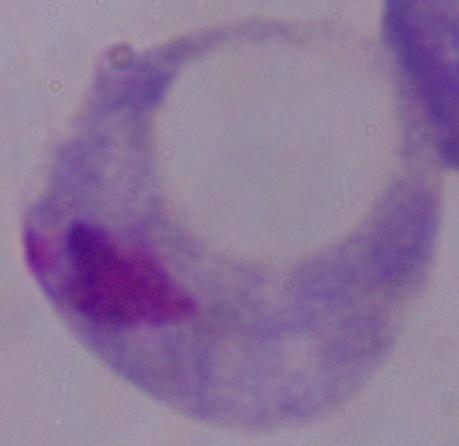
Summary:
  - Identification: trichomonad
  - Modality: photomicrograph
  - Magnification: 1000x